Identify the blood parasite species.
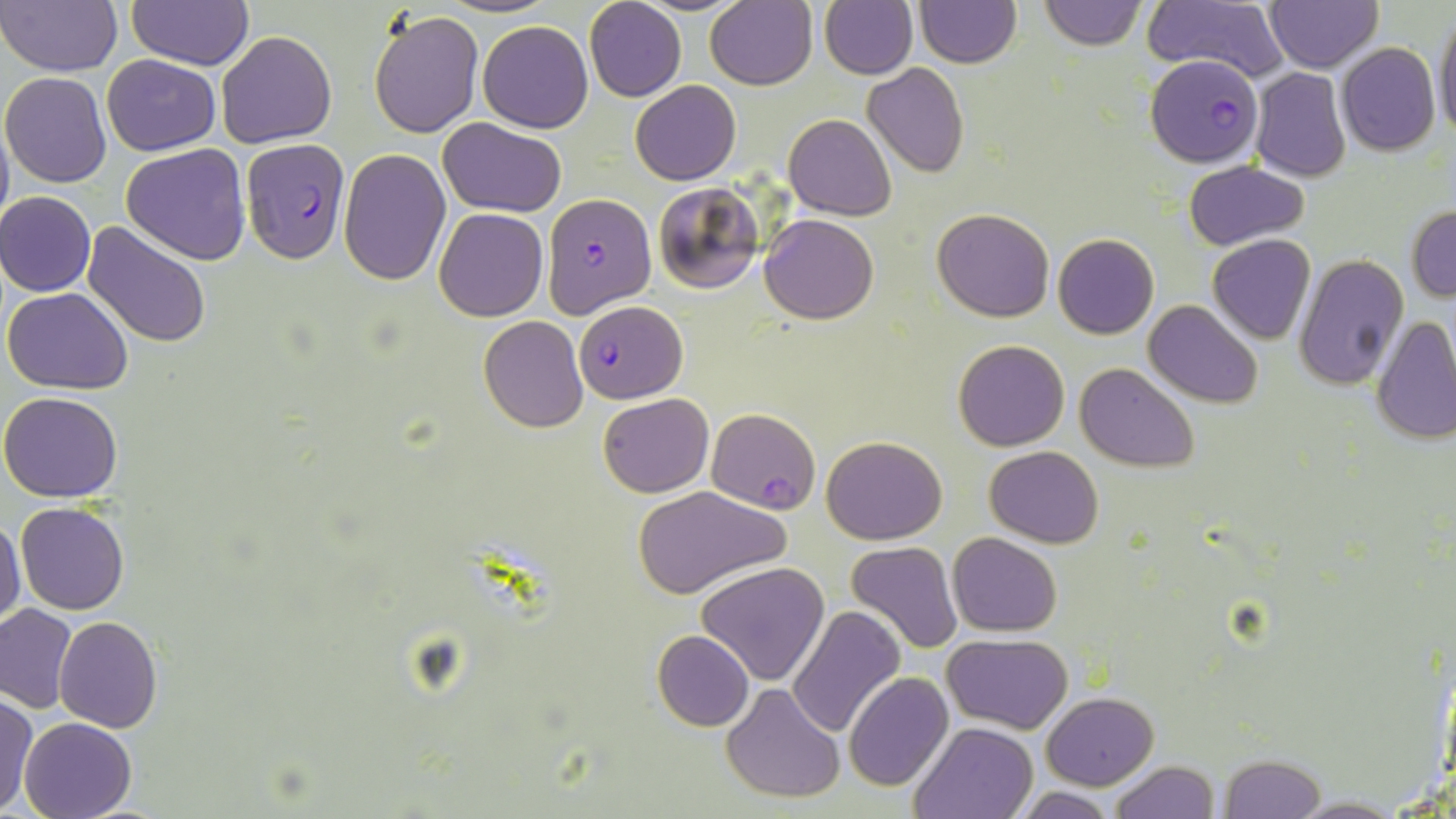

Plasmodium falciparum.

uninfected red blood cell locations = approximate bounding boxes as (x1, y1, x2, y2) in pixels: (1, 0, 125, 77), (439, 0, 553, 19), (583, 0, 687, 101), (705, 0, 817, 90), (915, 0, 1020, 68), (1039, 0, 1145, 49), (1143, 0, 1290, 84), (1265, 0, 1381, 72), (127, 1, 255, 70), (820, 1, 917, 79), (368, 8, 483, 138), (1433, 11, 1456, 144), (478, 21, 593, 133), (216, 30, 338, 148), (1337, 43, 1440, 156), (102, 54, 219, 155), (862, 63, 969, 179), (1250, 67, 1351, 182), (2, 72, 113, 187), (630, 80, 742, 185), (0, 105, 14, 238), (784, 114, 896, 220), (437, 118, 568, 218), (120, 144, 251, 265), (337, 149, 450, 285), (1183, 161, 1310, 248), (653, 181, 766, 295), (1, 191, 97, 297), (1407, 205, 1456, 302), (433, 207, 548, 321), (933, 208, 1054, 322), (759, 212, 878, 323), (82, 222, 212, 347), (1053, 233, 1159, 339), (1207, 234, 1315, 343), (1295, 254, 1409, 392), (3, 286, 134, 393), (1143, 298, 1264, 408), (478, 315, 588, 433), (1372, 316, 1456, 444), (954, 339, 1070, 450), (1073, 362, 1200, 473), (0, 391, 124, 502), (597, 393, 714, 496), (705, 407, 820, 514), (821, 435, 946, 544), (985, 445, 1103, 547), (631, 485, 787, 599), (16, 500, 129, 614), (0, 516, 26, 629), (947, 532, 1063, 637), (845, 540, 964, 653), (696, 561, 830, 686), (0, 604, 77, 713), (786, 605, 906, 737), (55, 617, 163, 732), (653, 630, 754, 731), (943, 633, 1072, 733), (843, 672, 954, 792), (721, 682, 844, 803), (1044, 692, 1158, 789), (1, 694, 37, 815), (19, 717, 137, 818), (911, 721, 1038, 818), (1218, 754, 1326, 819), (1109, 760, 1220, 818), (1011, 788, 1121, 818), (1287, 795, 1406, 817)
image size = 1456×819 pixels
modality = light microscopy
stain = May-Grünwald-Giemsa
field of view = one of a larger specimen
Plasmodium falciparum-infected red blood cell locations = approximate bounding boxes as (x1, y1, x2, y2) in pixels: (1147, 55, 1262, 168), (241, 138, 349, 264), (544, 192, 655, 318), (574, 301, 688, 404)
preparation = thin blood smear
magnification = 1000x